Point out each Plasmodium parasite.
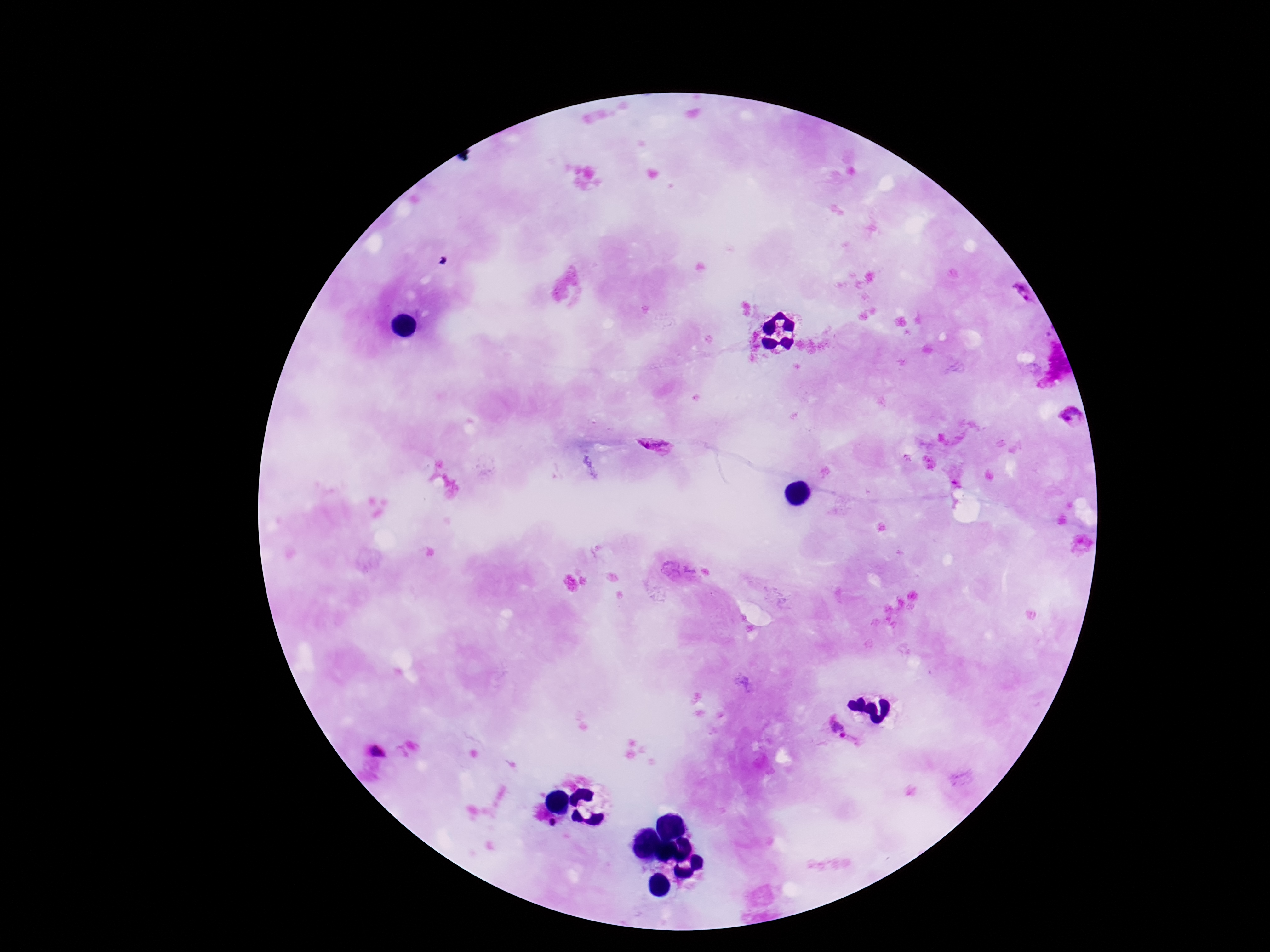
Approximate object centers, in pixels from the top-left corner.
Plasmodium parasites: (x=1025, y=295), (x=1070, y=416), (x=653, y=446), (x=837, y=728), (x=380, y=751).

One field from this slide. Image is 1270×952 pixels. Giemsa-stained preparation. Photographed through the microscope eyepiece with a smartphone camera. Thick peripheral-blood smear. Patient malaria status: positive. 100x magnification.